Describe the morphology of the red blood cells.
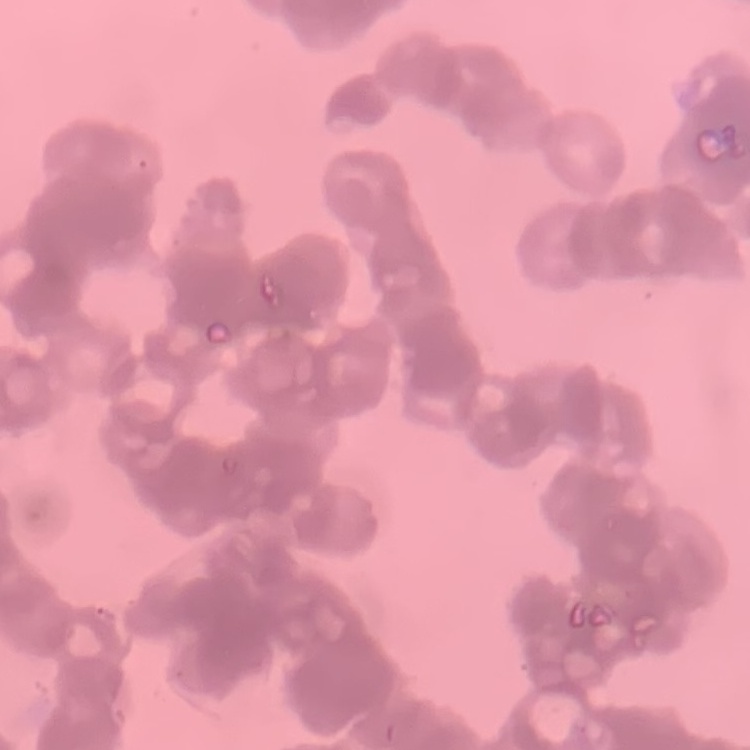

They show rouleaux formation.

preparation: thin peripheral smear
image_type: square crop of a larger photomicrograph
stain: Field's or Giemsa